Locate every P. falciparum parasite and identify its life-cycle stage.
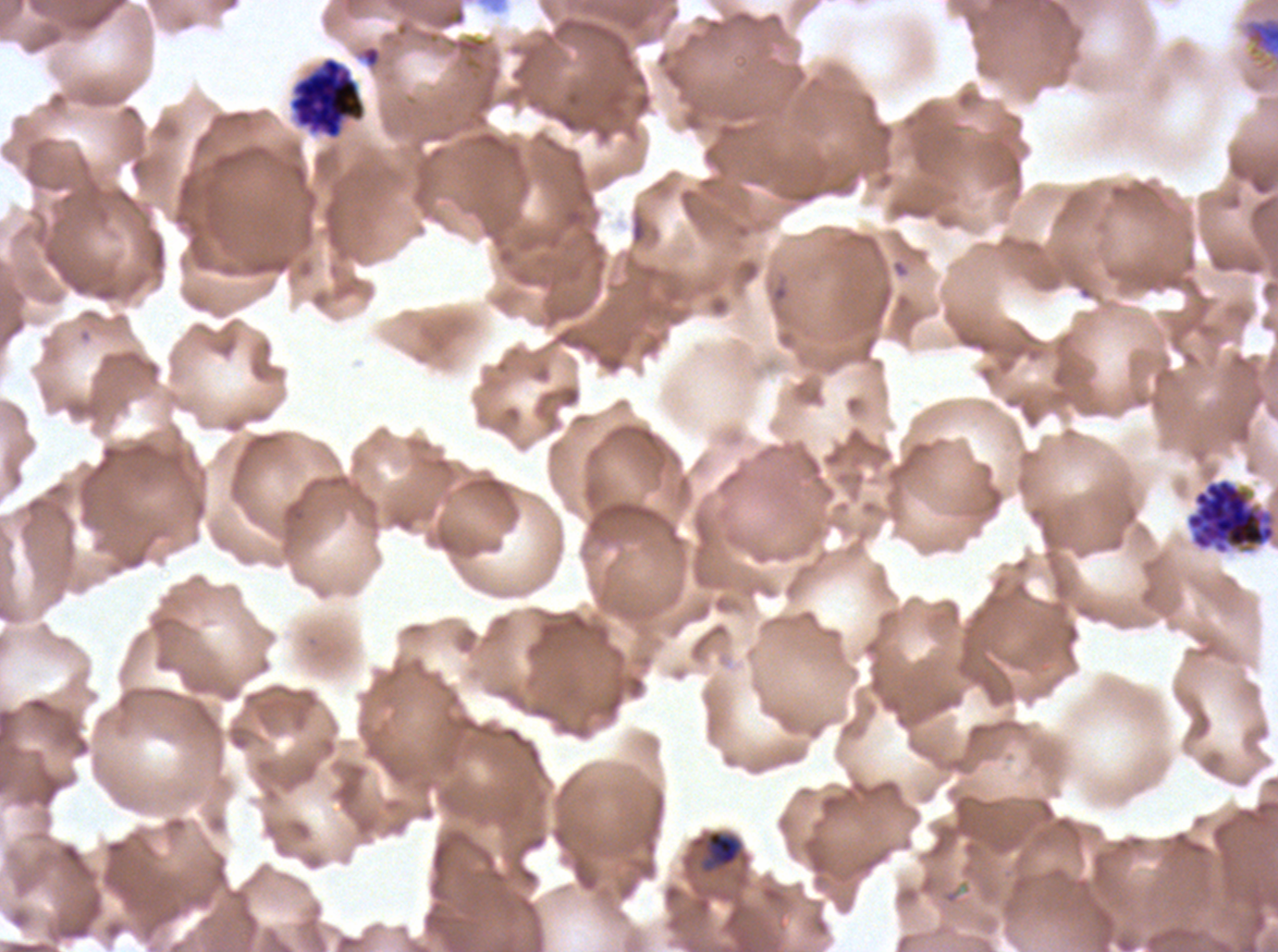

Approximate bounding boxes as [x1, y1, x2, y2] in pixels.
Late-ring/early-trophozoite forms: [690, 829, 744, 874].
Late trophozoites: [1241, 14, 1277, 72].
Segmenters: [289, 56, 366, 140], [1185, 477, 1277, 555].
No rings, mid trophozoites, early schizonts, late schizonts, or gametocytes observed.

Giemsa stain. A sub-image separated from a larger composite. Thin blood film. P. falciparum from a patient in The Gambia, cultured ex vivo for 24 to 48 hours. Image is 1278×952 pixels. Life-cycle stages observed: late-ring/early-trophozoite, late trophozoite, segmenter.